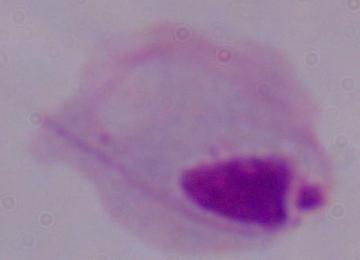
identification: trichomonad
modality: photomicrograph
magnification: 1000x